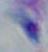
Summary:
  - Identification: Toxoplasma gondii
  - Modality: micrograph
  - Magnification: 1000x